Outline platelets.
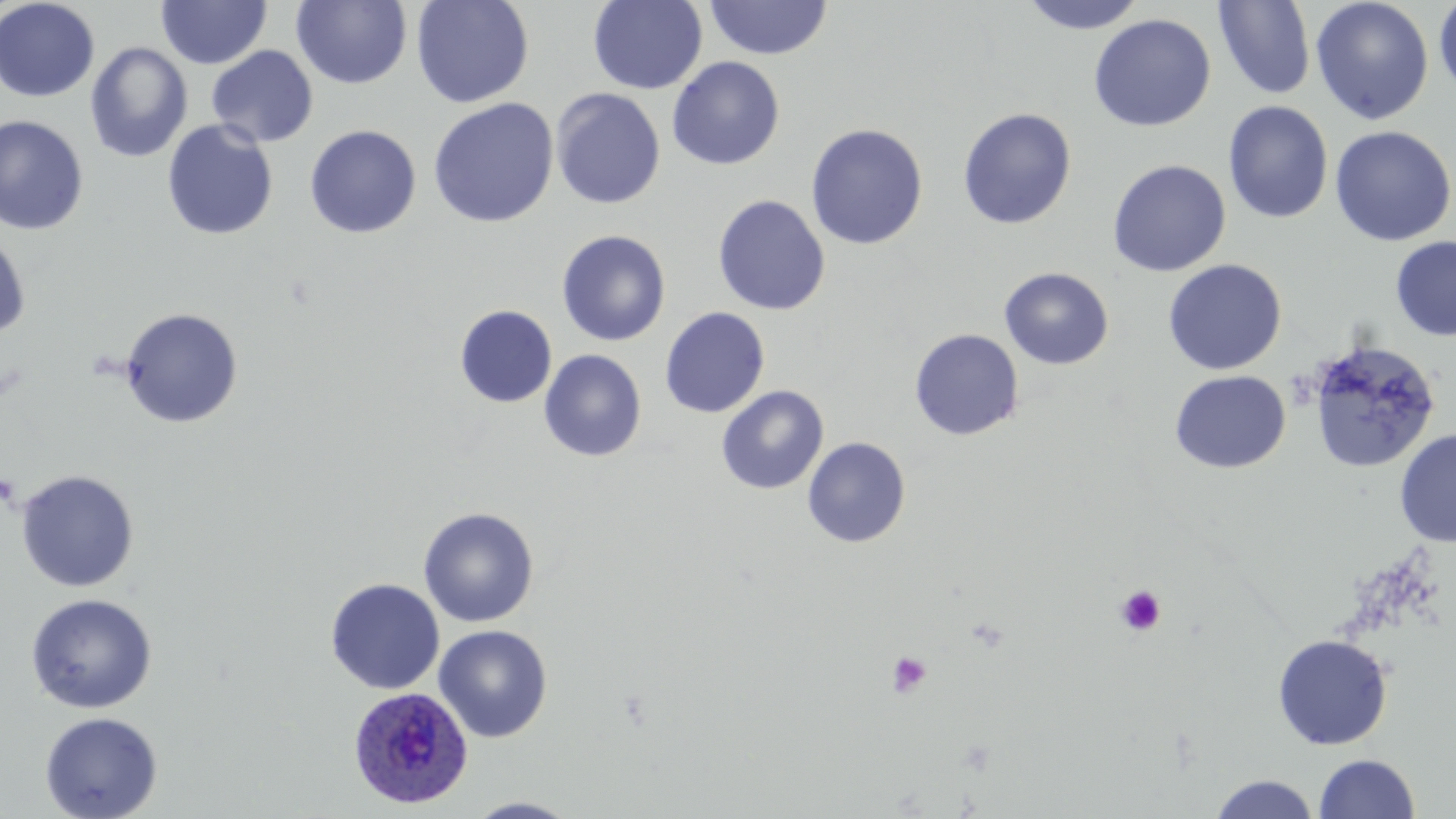

Approximate bounding boxes as named x1/y1/x2/y2 corners in pixels.
Platelets: (x1=1114, y1=584, x2=1166, y2=636), (x1=886, y1=650, x2=932, y2=698).

Uninfected red blood cell locations: (x1=0, y1=0, x2=100, y2=102), (x1=156, y1=0, x2=271, y2=69), (x1=411, y1=0, x2=534, y2=109), (x1=587, y1=0, x2=708, y2=94), (x1=704, y1=0, x2=832, y2=61), (x1=1020, y1=0, x2=1149, y2=33), (x1=1310, y1=0, x2=1434, y2=125), (x1=1433, y1=0, x2=1456, y2=98), (x1=291, y1=1, x2=412, y2=89), (x1=1213, y1=1, x2=1315, y2=100), (x1=1088, y1=14, x2=1216, y2=132), (x1=84, y1=42, x2=193, y2=162), (x1=206, y1=45, x2=318, y2=148), (x1=667, y1=56, x2=785, y2=171), (x1=550, y1=88, x2=665, y2=209), (x1=428, y1=98, x2=559, y2=228), (x1=1223, y1=101, x2=1333, y2=223), (x1=957, y1=107, x2=1076, y2=229), (x1=0, y1=115, x2=89, y2=235), (x1=1220, y1=115, x2=1453, y2=230), (x1=162, y1=120, x2=279, y2=240), (x1=806, y1=123, x2=928, y2=250), (x1=304, y1=124, x2=422, y2=238), (x1=1329, y1=125, x2=1455, y2=247), (x1=1107, y1=159, x2=1231, y2=276), (x1=712, y1=195, x2=830, y2=316), (x1=556, y1=230, x2=671, y2=346), (x1=0, y1=231, x2=31, y2=339), (x1=1390, y1=235, x2=1456, y2=342), (x1=1162, y1=259, x2=1287, y2=375), (x1=999, y1=267, x2=1114, y2=370), (x1=454, y1=305, x2=558, y2=408), (x1=119, y1=307, x2=244, y2=428), (x1=660, y1=307, x2=770, y2=418), (x1=909, y1=328, x2=1025, y2=441), (x1=1307, y1=339, x2=1441, y2=473), (x1=539, y1=349, x2=647, y2=462), (x1=1170, y1=370, x2=1291, y2=474), (x1=716, y1=385, x2=829, y2=495), (x1=1394, y1=428, x2=1455, y2=548), (x1=802, y1=436, x2=911, y2=548), (x1=15, y1=469, x2=140, y2=593), (x1=418, y1=507, x2=540, y2=627), (x1=325, y1=578, x2=446, y2=695), (x1=25, y1=592, x2=158, y2=714), (x1=433, y1=625, x2=553, y2=742), (x1=1272, y1=634, x2=1393, y2=750), (x1=39, y1=711, x2=163, y2=819), (x1=1314, y1=753, x2=1420, y2=818), (x1=1208, y1=774, x2=1321, y2=818), (x1=464, y1=797, x2=582, y2=818). Plasmodium ovale-infected red blood cell locations: (x1=348, y1=686, x2=473, y2=809). Slide-level diagnosis: Plasmodium ovale. One field of a larger specimen. 1000x magnification. Image is 1456×819 pixels. May-Grünwald-Giemsa-stained preparation. Light microscopy. Thin blood film.